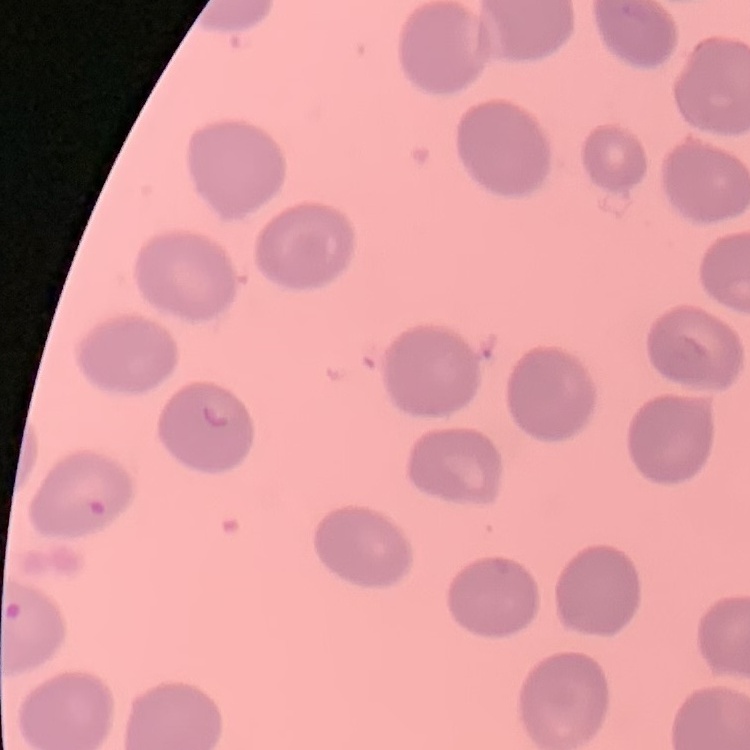

red blood cell morphology = no rouleaux formation
image type = one tile cut from a larger photomicrograph
stain = Field's or Giemsa
preparation = thin peripheral smear